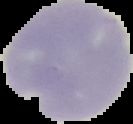

Malaria status: uninfected. From a thin blood smear. Cell region segmented out of the field of view; the surrounding area is masked to black. Image is 133×124 pixels.